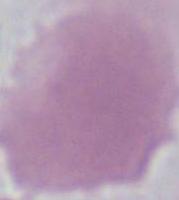

{
  "identification": "red blood cell",
  "magnification": "1000x",
  "modality": "photomicrograph"
}